Comment on the morphology of the red blood cells.
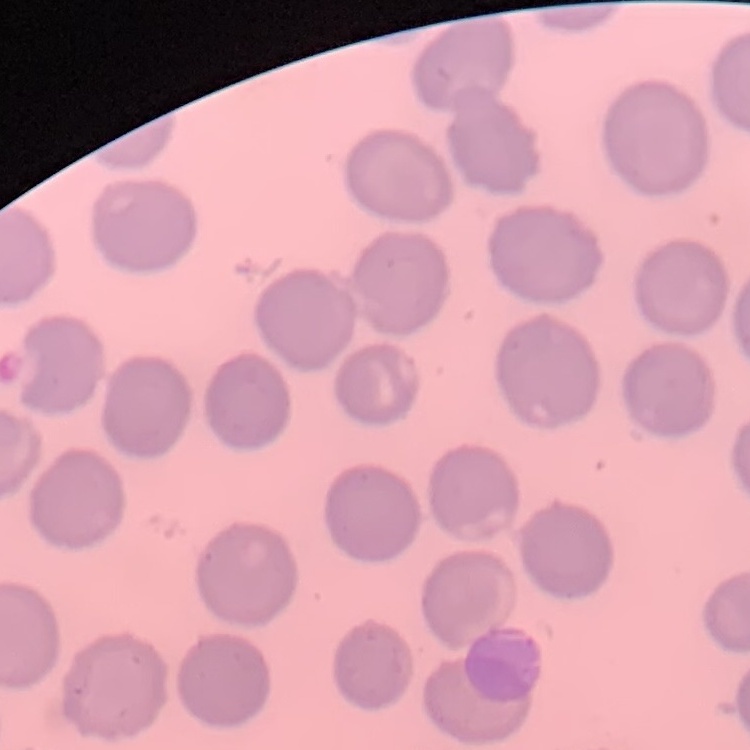

They show no rouleaux formation.

Thin blood smear. Square crop of a larger photomicrograph. Field's or Giemsa stain.